Report the malaria status of this cell.
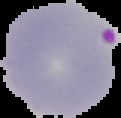
Parasitized.

From a thin blood film. Image is 121×118 pixels. Segmented cell region on a black background.